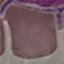

malaria status = uninfected
preparation = thin blood film
capture = smartphone through the microscope eyepiece
image type = automatically extracted cell patch, resized to 64 × 64 pixels
stain = Giemsa